Report the malaria status of this cell.
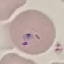
Uninfected.

preparation = thin blood smear
image type = cell patch, automatically extracted from a larger field of view and resized to 64 × 64 pixels
capture = smartphone through the microscope eyepiece
stain = Giemsa